Outline each P. falciparum parasite and classify it by life-cycle stage.
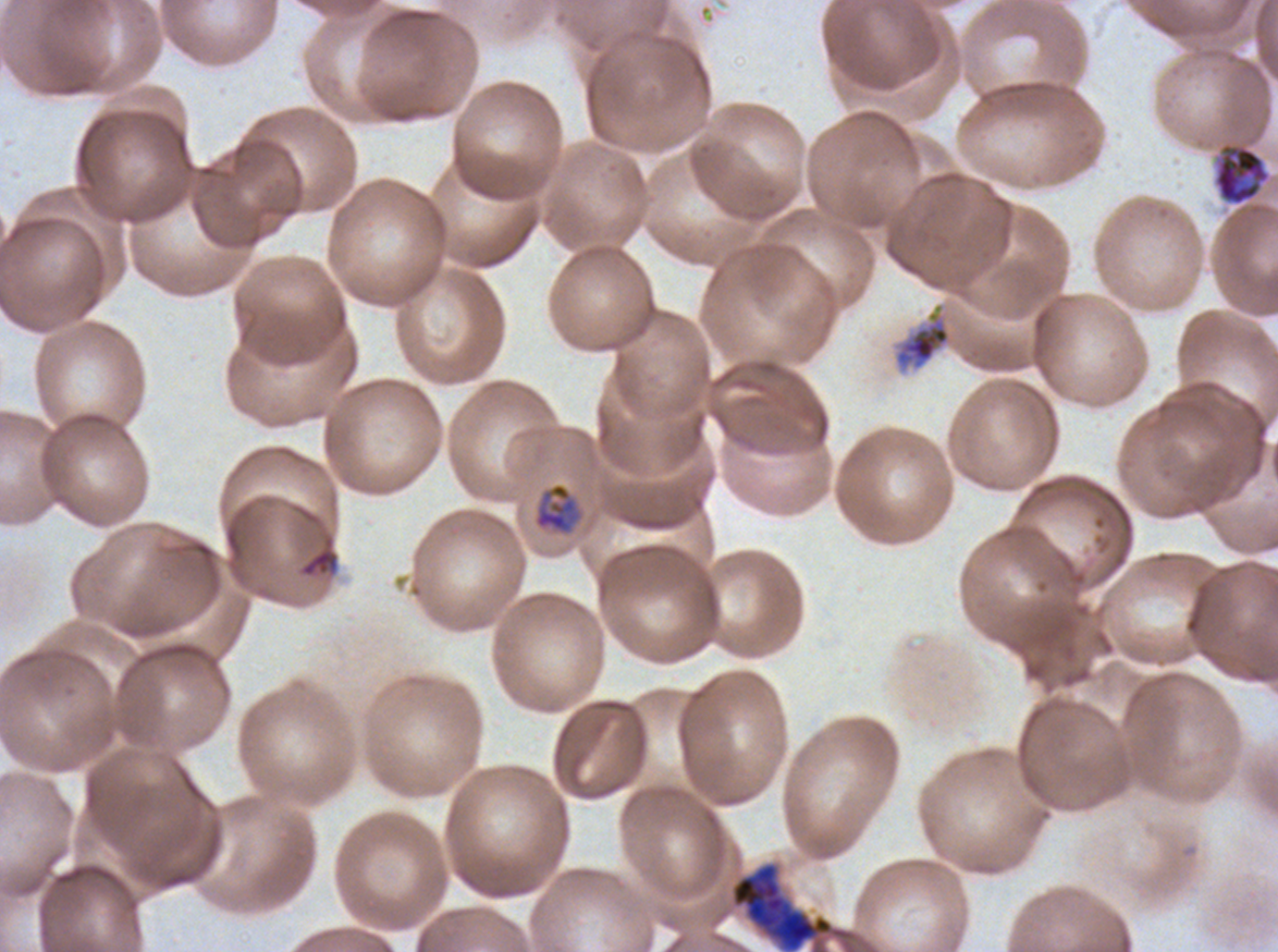
Approximate bounding rectangles given as corner coordinates in pixels from the top-left.
Mid trophozoites: (x1=534, y1=482, x2=579, y2=534).
Early schizonts: (x1=731, y1=861, x2=834, y2=951).
Segmenters: (x1=1212, y1=141, x2=1272, y2=207).
No rings, late-ring/early-trophozoite forms, late trophozoites, late schizonts, or gametocytes observed.

Debris locations: (x1=892, y1=301, x2=952, y2=373), (x1=300, y1=548, x2=338, y2=577). P. falciparum cultured ex vivo for 24 to 48 hours, from a patient in The Gambia. Thin blood film. Image is 1278×952 pixels. A sub-image separated from a larger composite. Life-cycle stages observed: mid trophozoite, early schizont, segmenter. Giemsa stain.